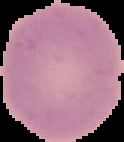
Segmented cell region on a black background. Image is 124×142 pixels. Result: no malaria parasites seen. From a thin blood film.